Report the malaria status of this cell.
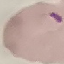

It is parasitized.

stain: Giemsa
image_type: cell patch, automatically extracted from a larger field of view and resized to 64 × 64 pixels
preparation: thin smear
capture: smartphone through the microscope eyepiece